Name the cell type shown.
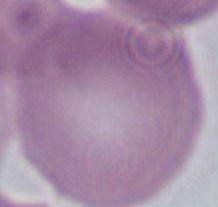

This is an erythrocyte.

modality = micrograph
magnification = 1000x